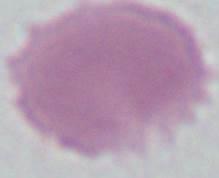
Photomicrograph. Captured at 1000x magnification. An erythrocyte is seen.